Locate every Plasmodium falciparum-infected red blood cell.
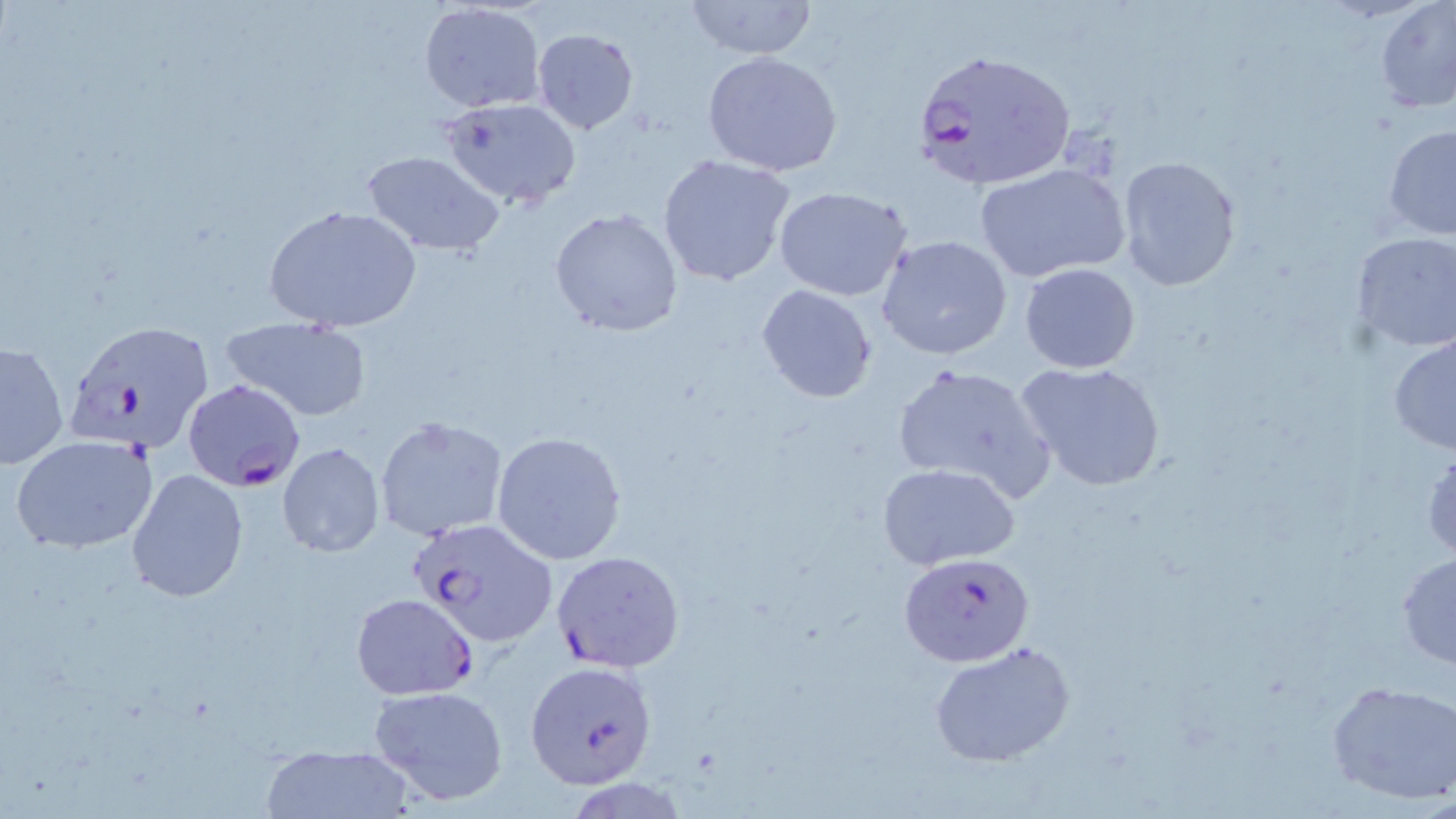

Approximate bounding boxes as named x1/y1/x2/y2 corners in pixels.
Plasmodium falciparum-infected red blood cells: (x1=911, y1=48, x2=1076, y2=192), (x1=61, y1=319, x2=214, y2=457), (x1=183, y1=377, x2=305, y2=492), (x1=407, y1=517, x2=559, y2=648), (x1=551, y1=550, x2=684, y2=673), (x1=900, y1=552, x2=1034, y2=667), (x1=352, y1=594, x2=477, y2=699), (x1=525, y1=660, x2=657, y2=790).

Uninfected red blood cell locations: (x1=1375, y1=0, x2=1456, y2=111), (x1=419, y1=2, x2=545, y2=114), (x1=680, y1=2, x2=820, y2=58), (x1=533, y1=29, x2=640, y2=134), (x1=701, y1=50, x2=846, y2=176), (x1=442, y1=97, x2=580, y2=210), (x1=1383, y1=125, x2=1456, y2=240), (x1=360, y1=150, x2=505, y2=258), (x1=657, y1=155, x2=798, y2=289), (x1=1116, y1=155, x2=1243, y2=293), (x1=974, y1=163, x2=1131, y2=284), (x1=772, y1=184, x2=914, y2=301), (x1=261, y1=204, x2=424, y2=335), (x1=549, y1=208, x2=684, y2=338), (x1=1351, y1=233, x2=1456, y2=353), (x1=876, y1=234, x2=1014, y2=360), (x1=1019, y1=262, x2=1141, y2=375), (x1=755, y1=285, x2=876, y2=403), (x1=221, y1=316, x2=372, y2=422), (x1=1387, y1=335, x2=1456, y2=456), (x1=1, y1=340, x2=69, y2=468), (x1=1015, y1=360, x2=1168, y2=492), (x1=889, y1=361, x2=1057, y2=503), (x1=374, y1=416, x2=508, y2=541), (x1=491, y1=431, x2=627, y2=564), (x1=11, y1=435, x2=157, y2=554), (x1=277, y1=442, x2=385, y2=557), (x1=1422, y1=443, x2=1456, y2=564), (x1=877, y1=462, x2=1021, y2=569), (x1=126, y1=468, x2=248, y2=602), (x1=1395, y1=551, x2=1456, y2=669), (x1=930, y1=640, x2=1077, y2=768), (x1=1324, y1=681, x2=1456, y2=805), (x1=369, y1=684, x2=510, y2=806), (x1=262, y1=747, x2=413, y2=818). Slide-level diagnosis: Plasmodium falciparum. Thin blood film. Optical microscopy. Image is 1456×819 pixels. May-Grünwald-Giemsa stain. 1000x magnification. One field of a larger specimen.